Report the malaria status of this cell.
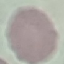

It is uninfected.

{
  "stain": "Giemsa",
  "capture": "smartphone camera at the microscope eyepiece",
  "image_type": "automatically extracted cell patch, resized to 64 × 64 pixels",
  "preparation": "thin smear"
}